Assess the morphology of the erythrocytes.
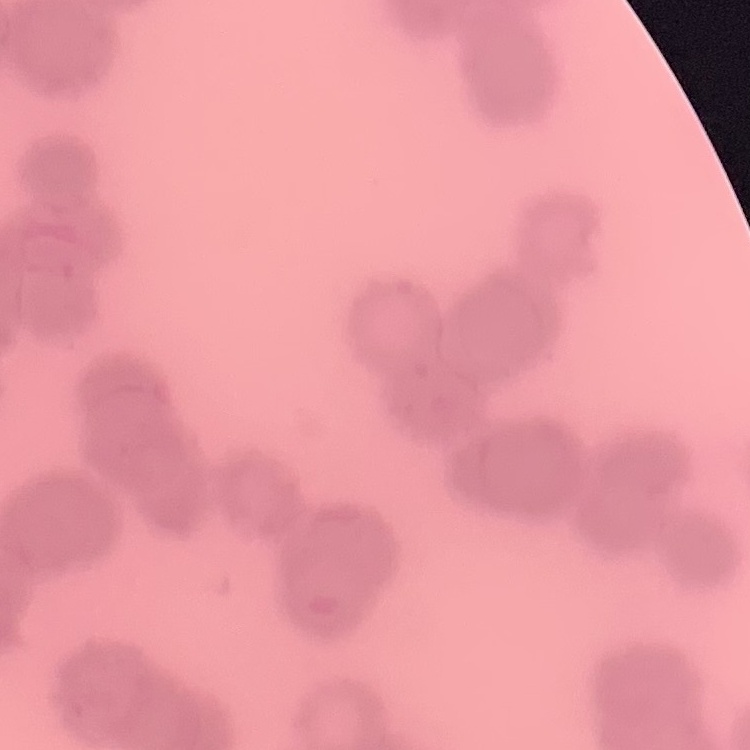
They show rouleaux formation.

image type = square crop of a larger photomicrograph
preparation = thin peripheral smear
stain = Field's or Giemsa